Describe the morphology of the red blood cells.
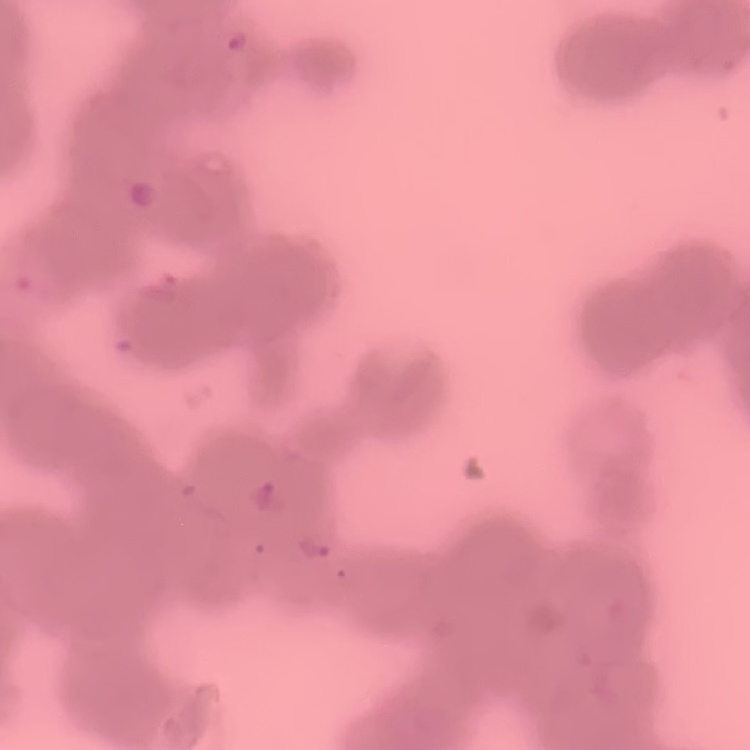

Rouleaux formation.

Summary:
  - Preparation: thin blood film
  - Stain: Field's or Giemsa
  - Image type: square crop of a larger photomicrograph